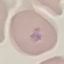
Summary:
  - Malaria status: parasitized
  - Stain: Giemsa
  - Preparation: thin blood smear
  - Image type: automatically extracted cell patch, resized to 64 × 64 pixels
  - Capture: smartphone camera at the microscope eyepiece